Comment on the morphology of the red blood cells.
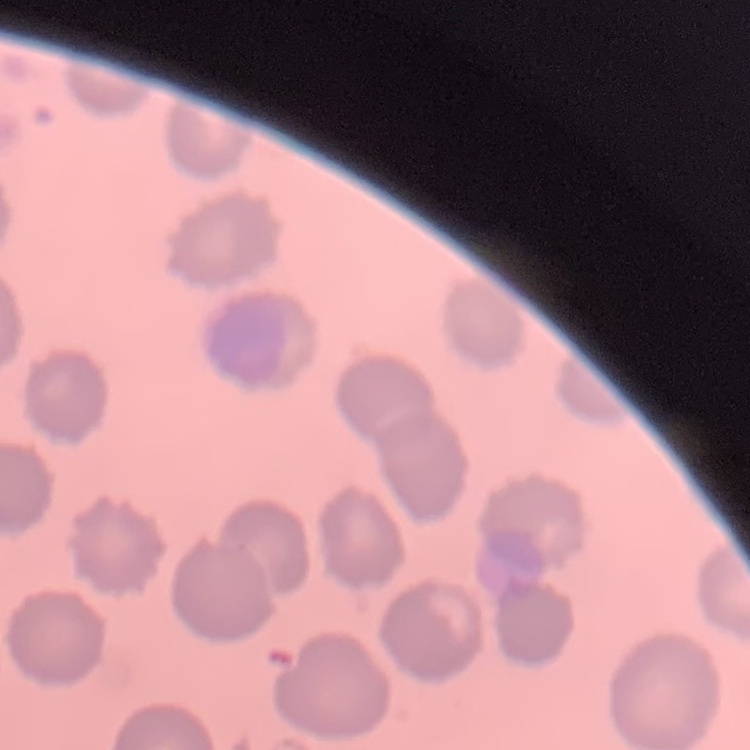
No rouleaux formation.

image type = square crop of a larger photomicrograph
preparation = thin blood smear
stain = Field's or Giemsa